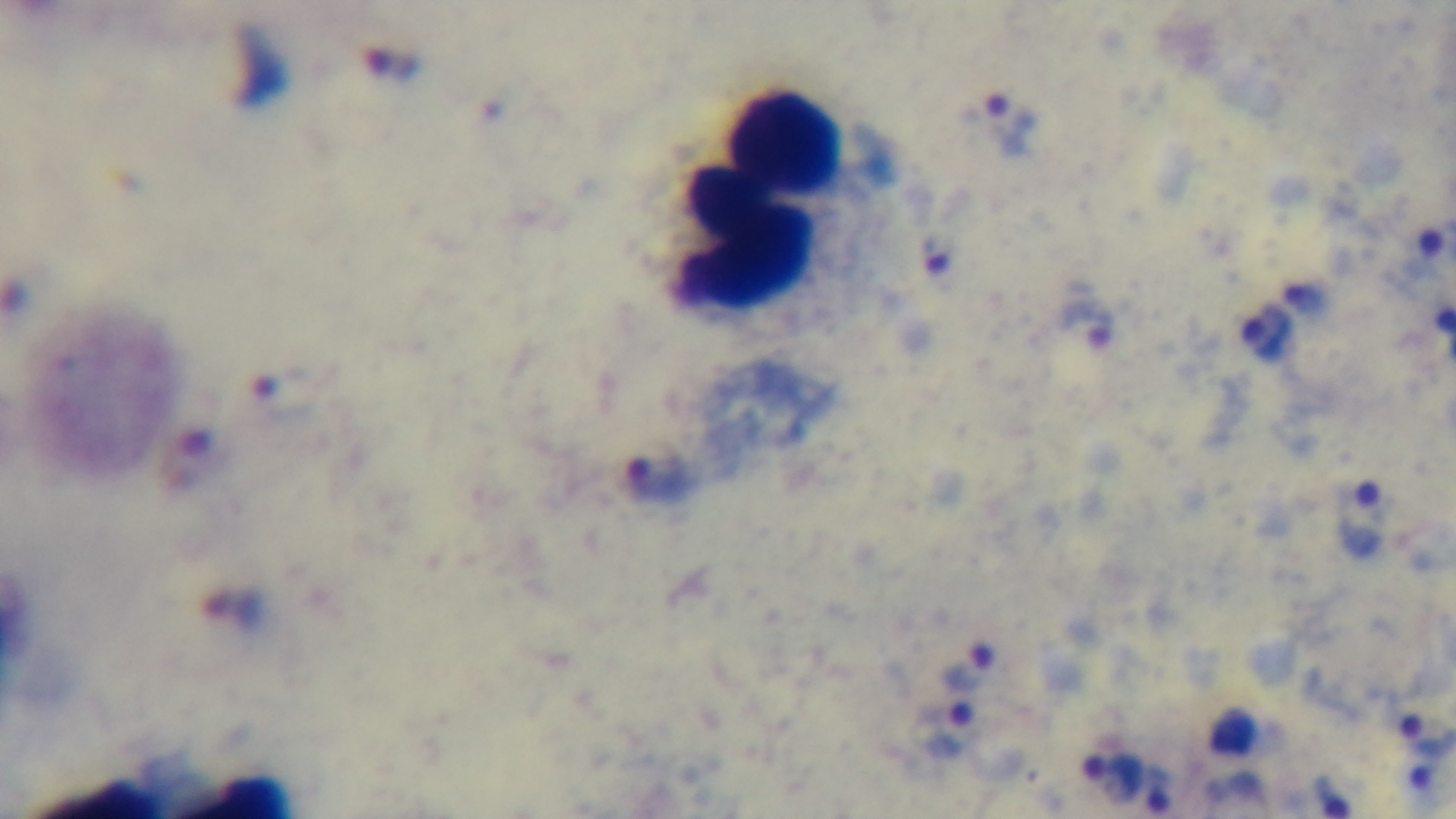

Summary:
  - Malaria status: positive
  - Stain: Giemsa
  - Objective: 100x oil immersion
  - Modality: light microscopy
  - Field of view: single
  - Preparation: thick blood film
  - Capture: mounted 4K digital camera